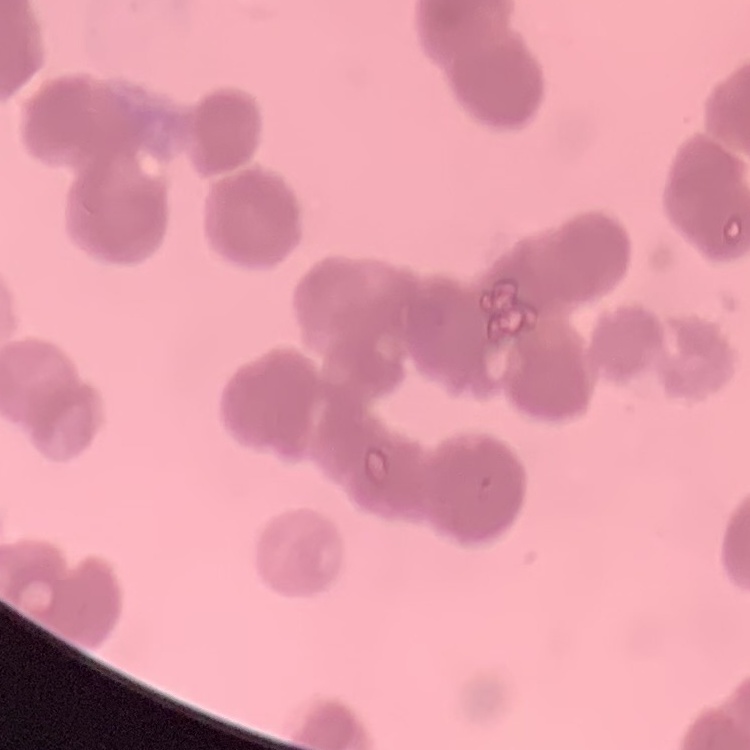
erythrocyte_morphology: rouleaux formation
stain: Field's or Giemsa
preparation: thin blood film
image_type: one tile cut from a larger photomicrograph